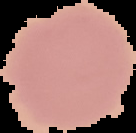
Summary:
  - Image size: 136×133 pixels
  - Image type: segmented cell region on a black background
  - Preparation: thin blood smear
  - Result: no malaria parasites detected